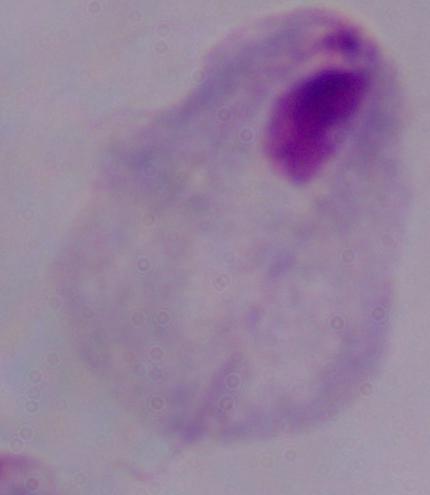

{
  "identification": "trichomonad",
  "magnification": "1000x",
  "modality": "micrograph"
}